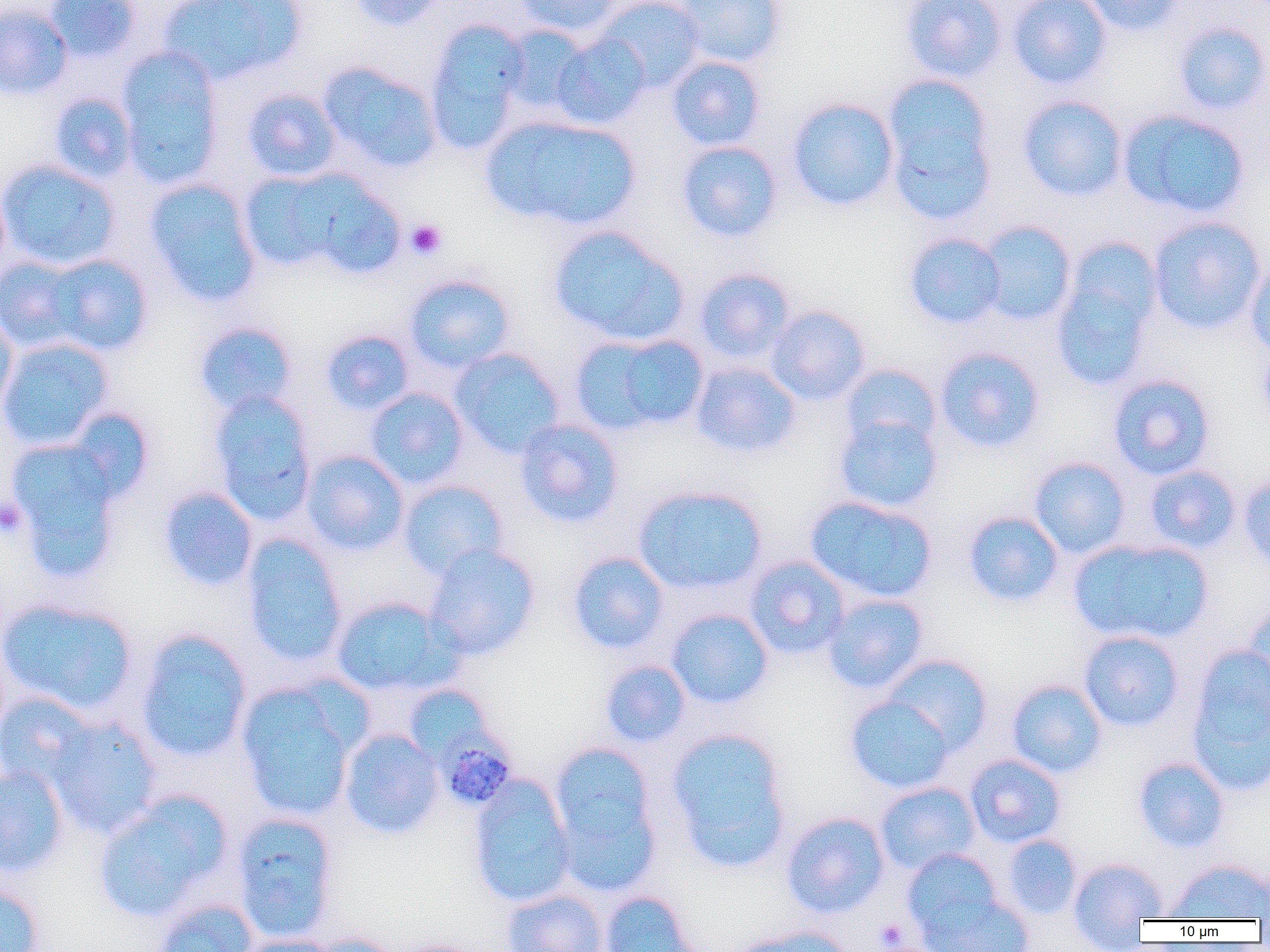

Summary:
  - Coordinate format: approximate bounding boxes as (x1, y1, x2, y2) in pixels
  - Plasmodium malariae-infected red blood cell locations: (437, 732, 517, 811)
  - Platelet locations: (405, 219, 447, 260), (0, 499, 28, 537), (874, 918, 910, 950)
  - Uninfected red blood cell locations: (43, 0, 141, 61), (159, 0, 305, 85), (349, 0, 447, 31), (513, 0, 625, 38), (596, 0, 706, 90), (675, 0, 786, 67), (900, 0, 1007, 82), (1007, 0, 1112, 89), (1080, 0, 1186, 36), (0, 3, 73, 100), (424, 18, 532, 152), (1172, 21, 1270, 116), (551, 34, 650, 130), (116, 47, 225, 189), (666, 55, 766, 150), (317, 61, 443, 172), (881, 77, 998, 225), (242, 87, 342, 182), (48, 91, 138, 183), (1017, 95, 1128, 201), (786, 98, 899, 211), (1118, 108, 1251, 219), (480, 114, 642, 230), (676, 140, 783, 243), (0, 159, 122, 271), (239, 170, 344, 271), (296, 170, 406, 278), (144, 178, 263, 307), (0, 180, 11, 285), (1148, 217, 1266, 335), (976, 220, 1077, 326), (548, 224, 689, 346), (904, 232, 1007, 329), (1050, 242, 1163, 392), (42, 253, 154, 356), (0, 255, 87, 353), (1245, 256, 1270, 361), (693, 267, 795, 364), (403, 273, 516, 372), (766, 305, 871, 405), (0, 311, 18, 414), (194, 321, 298, 416), (320, 328, 415, 416), (569, 331, 709, 436), (0, 337, 113, 450), (1257, 344, 1270, 431), (934, 346, 1046, 453), (450, 348, 565, 457), (691, 362, 801, 458), (839, 363, 942, 452), (1107, 373, 1216, 480), (365, 387, 469, 489), (208, 390, 318, 526), (66, 408, 155, 502), (833, 413, 943, 513), (515, 418, 624, 527), (6, 439, 123, 579), (301, 450, 410, 555), (1029, 456, 1131, 558), (1144, 465, 1241, 554), (1238, 474, 1270, 575), (397, 480, 509, 580), (633, 484, 768, 594), (158, 486, 258, 591), (805, 495, 937, 603), (962, 511, 1064, 608), (241, 535, 348, 668), (1067, 537, 1214, 646), (423, 544, 541, 660), (567, 551, 670, 654), (744, 556, 851, 659), (822, 593, 929, 694), (331, 596, 461, 697), (0, 597, 138, 715), (1244, 600, 1270, 702), (666, 608, 774, 709), (135, 628, 253, 763), (1078, 630, 1185, 732), (1186, 643, 1270, 794), (882, 654, 993, 754), (599, 659, 691, 748), (1006, 679, 1107, 778), (403, 684, 493, 764), (236, 685, 358, 822), (0, 691, 97, 791), (845, 695, 954, 794), (46, 716, 164, 838), (665, 727, 793, 872), (339, 728, 444, 838), (547, 741, 663, 892), (964, 753, 1066, 848), (1132, 755, 1230, 854), (0, 765, 69, 877), (468, 774, 577, 908), (875, 781, 981, 875), (93, 791, 232, 922), (231, 811, 339, 943), (780, 811, 890, 919), (1001, 834, 1082, 920), (901, 847, 1003, 938), (1068, 857, 1167, 944), (1165, 858, 1270, 922), (0, 883, 46, 952), (501, 888, 609, 952), (599, 891, 701, 952), (922, 893, 1035, 952), (152, 898, 258, 952), (732, 926, 855, 952), (300, 932, 402, 952), (234, 934, 339, 952), (392, 939, 486, 952)
  - Slide-level diagnosis: Plasmodium malariae
  - Preparation: thin blood smear
  - Image size: 1270×952 pixels
  - Field of view: one of a larger specimen
  - Magnification: 1000x
  - Modality: light microscopy